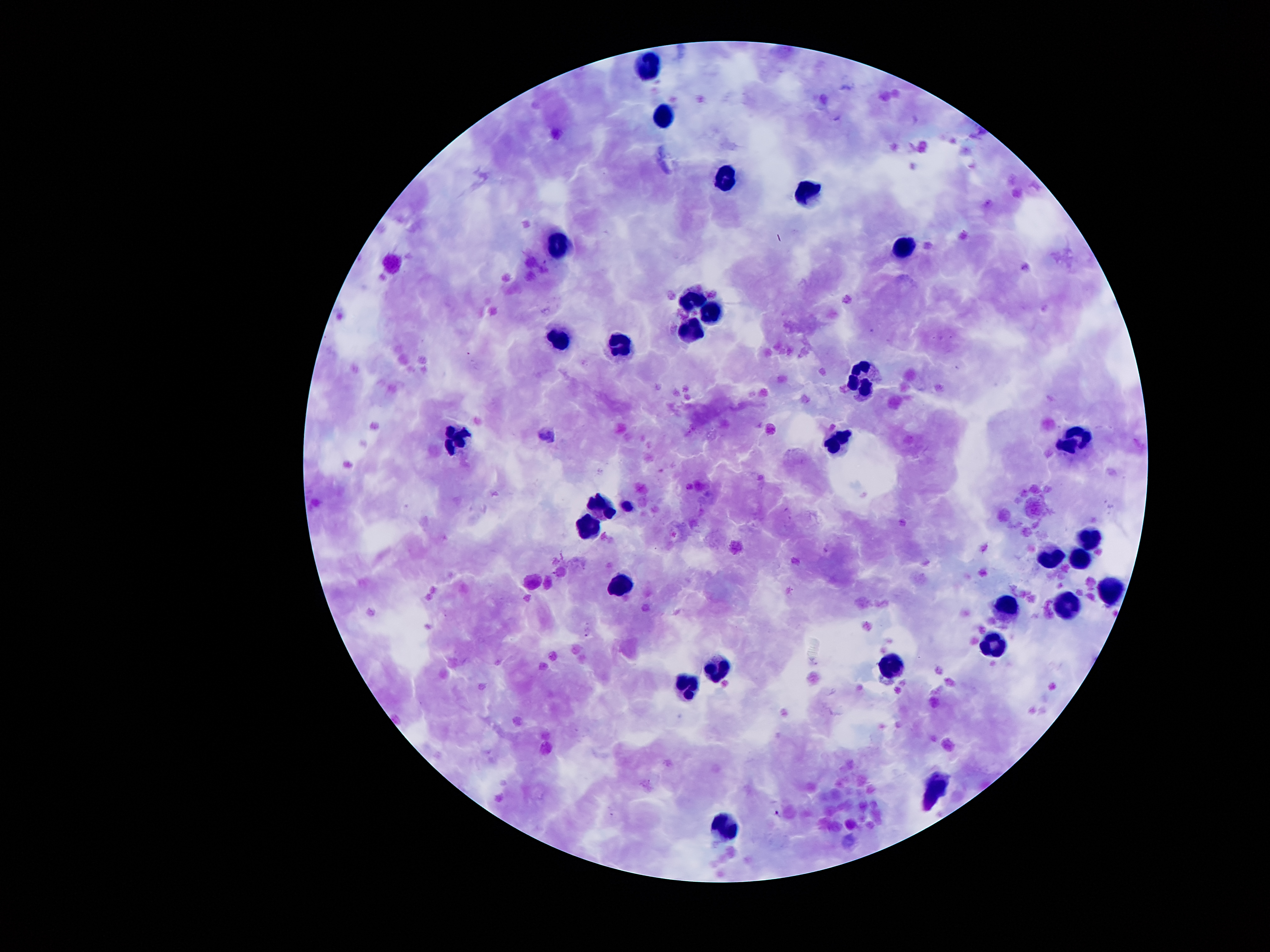 Approximate centers as {x, y} in pixels. Leukocyte locations: {650, 65}, {665, 115}, {725, 178}, {807, 190}, {557, 247}, {903, 248}, {688, 301}, {711, 310}, {688, 329}, {560, 340}, {621, 346}, {866, 381}, {1073, 434}, {458, 436}, {839, 436}, {603, 505}, {588, 523}, {1089, 536}, {1081, 555}, {1052, 556}, {620, 588}, {1110, 589}, {1066, 603}, {1009, 606}, {990, 643}, {888, 665}, {722, 666}, {690, 684}, {936, 787}, {726, 822}. Malaria parasite locations: {588, 632}, {777, 813}. 100x magnification. One field from this slide. Giemsa stain. Image is 1270×952 pixels. Patient malaria status: positive for Plasmodium falciparum. Thick blood film. Photographed through the microscope eyepiece with a smartphone camera.